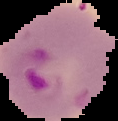 Image is 118×121 pixels. Cell region segmented out of the field of view; the surrounding area is masked to black. From a thin blood smear. Malaria status: parasitized.